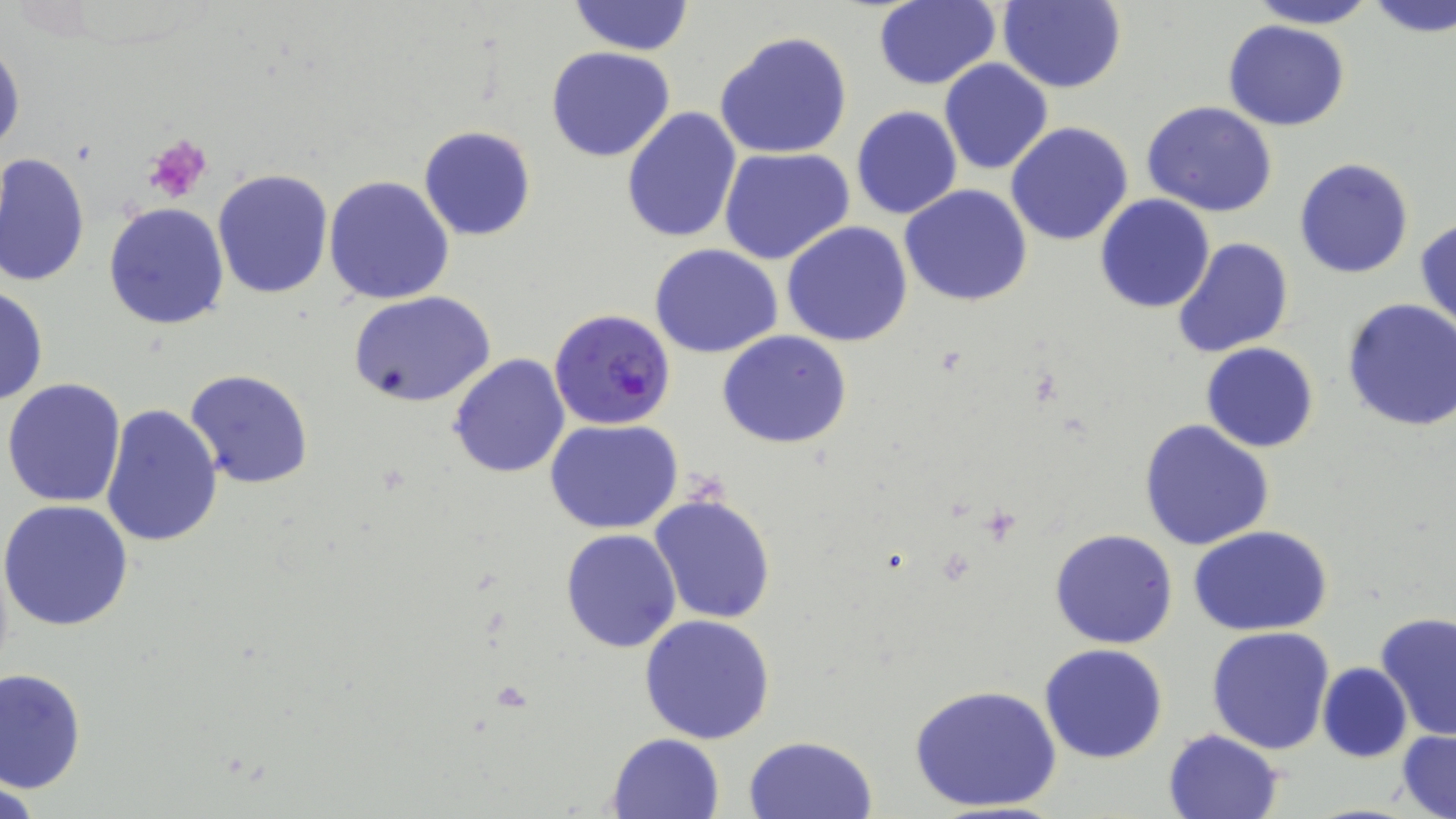
Approximate bounding boxes as named x1/y1/x2/y2 corners in pixels. Platelet locations: (x1=145, y1=136, x2=213, y2=203). Uninfected red blood cell locations: (x1=567, y1=0, x2=693, y2=56), (x1=872, y1=0, x2=1001, y2=90), (x1=996, y1=0, x2=1127, y2=93), (x1=1245, y1=0, x2=1378, y2=28), (x1=1365, y1=0, x2=1456, y2=38), (x1=1223, y1=19, x2=1349, y2=130), (x1=715, y1=30, x2=855, y2=160), (x1=1, y1=39, x2=24, y2=159), (x1=546, y1=46, x2=677, y2=163), (x1=938, y1=58, x2=1053, y2=175), (x1=1141, y1=101, x2=1280, y2=219), (x1=851, y1=106, x2=962, y2=220), (x1=622, y1=108, x2=744, y2=246), (x1=1005, y1=121, x2=1133, y2=246), (x1=418, y1=125, x2=537, y2=241), (x1=719, y1=146, x2=855, y2=266), (x1=1, y1=152, x2=91, y2=288), (x1=1295, y1=158, x2=1414, y2=279), (x1=212, y1=168, x2=335, y2=298), (x1=323, y1=176, x2=455, y2=305), (x1=899, y1=184, x2=1033, y2=307), (x1=1093, y1=194, x2=1216, y2=313), (x1=104, y1=202, x2=229, y2=329), (x1=1416, y1=218, x2=1456, y2=335), (x1=782, y1=222, x2=913, y2=348), (x1=1172, y1=236, x2=1294, y2=357), (x1=650, y1=244, x2=783, y2=359), (x1=0, y1=285, x2=48, y2=407), (x1=350, y1=291, x2=496, y2=408), (x1=1341, y1=298, x2=1456, y2=433), (x1=718, y1=329, x2=853, y2=449), (x1=1200, y1=342, x2=1320, y2=453), (x1=447, y1=353, x2=570, y2=478), (x1=184, y1=370, x2=314, y2=491), (x1=4, y1=378, x2=127, y2=507), (x1=100, y1=403, x2=224, y2=548), (x1=1138, y1=419, x2=1275, y2=553), (x1=545, y1=420, x2=683, y2=534), (x1=650, y1=494, x2=776, y2=624), (x1=1, y1=498, x2=133, y2=633), (x1=1190, y1=526, x2=1332, y2=637), (x1=559, y1=528, x2=681, y2=653), (x1=1049, y1=528, x2=1178, y2=649), (x1=1375, y1=610, x2=1456, y2=742), (x1=639, y1=614, x2=776, y2=743), (x1=1206, y1=627, x2=1336, y2=755), (x1=1039, y1=643, x2=1169, y2=764), (x1=1317, y1=663, x2=1411, y2=763), (x1=1, y1=668, x2=86, y2=792), (x1=908, y1=682, x2=1064, y2=814), (x1=1163, y1=728, x2=1284, y2=818), (x1=1397, y1=729, x2=1456, y2=819), (x1=607, y1=733, x2=727, y2=819), (x1=743, y1=735, x2=877, y2=818). Plasmodium falciparum-infected red blood cell locations: (x1=548, y1=307, x2=677, y2=431). Slide-level diagnosis: Plasmodium falciparum. Captured at 1000x magnification. May-Grünwald-Giemsa-stained preparation. Light microscopy. Image is 1456×819 pixels. Thin blood smear. One field of a larger specimen.